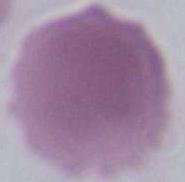

Summary:
  - Identification: erythrocyte
  - Modality: micrograph
  - Magnification: 1000x